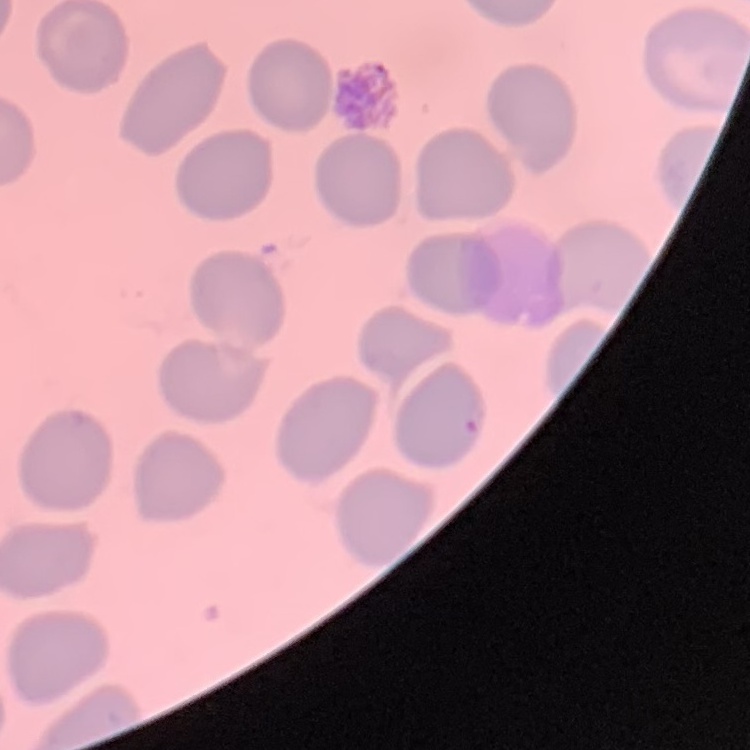
The erythrocytes show no rouleaux formation. Stained with either Field's or Giemsa. Thin peripheral smear. One tile cut from a larger photomicrograph.